Locate every Plasmodium parasite.
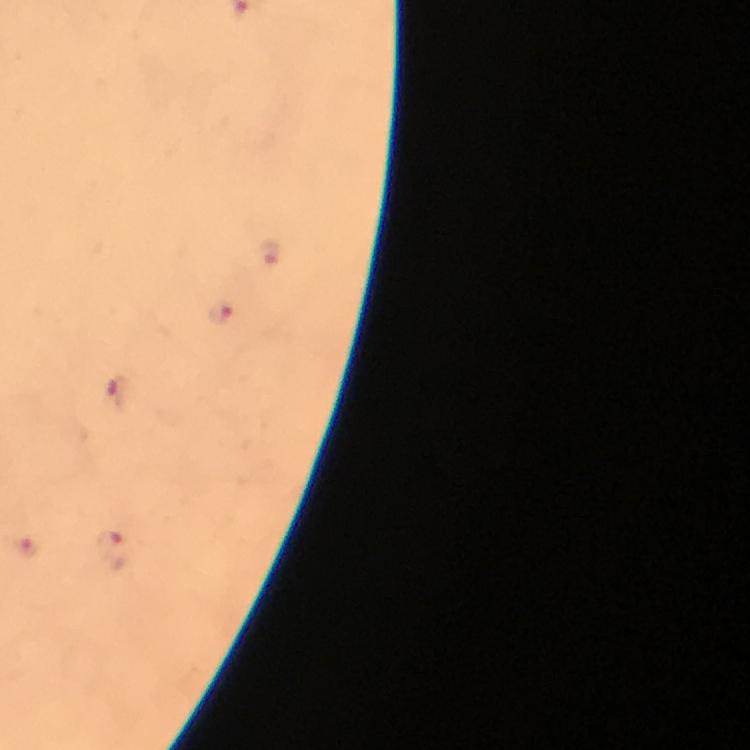
Approximate centers as {x, y} in pixels.
Plasmodium parasites: {269, 252}, {221, 315}, {115, 392}, {27, 548}, {111, 549}.

{
  "cropped_from": "a single field of view",
  "capture": "smartphone camera through the microscope",
  "preparation": "thick blood film",
  "immersion_oil": "applied",
  "magnification": "100x",
  "stain": "Giemsa",
  "context": "from a malaria diagnostic workup",
  "image_size": "750×750 pixels"
}